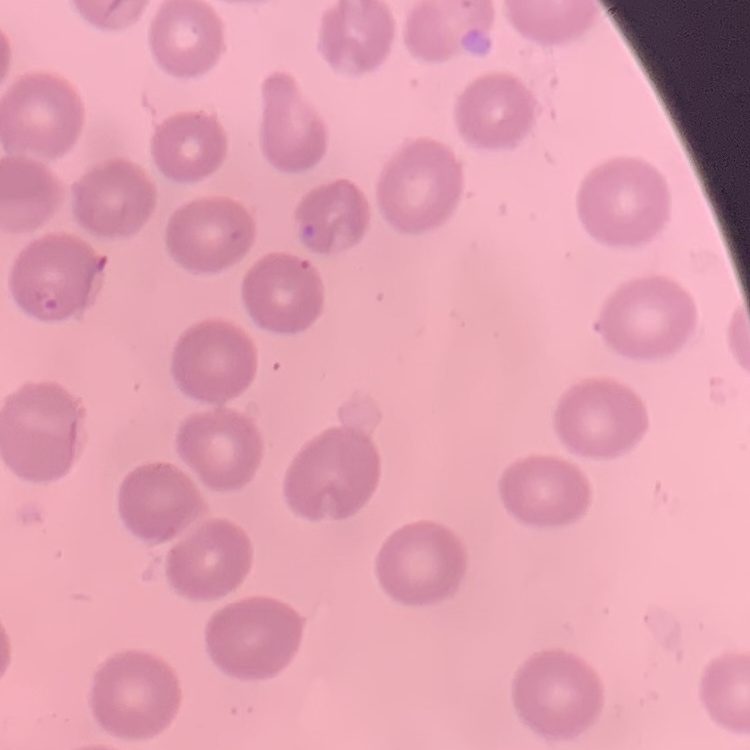

The erythrocytes show no rouleaux formation. Field's or Giemsa stain. Thin peripheral smear. Square crop of a larger photomicrograph.